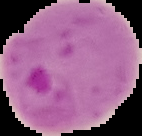

Summary:
  - Preparation: thin blood film
  - Image type: segmented cell region on a black background
  - Malaria status: parasitized
  - Image size: 142×136 pixels